Identify the parasite.
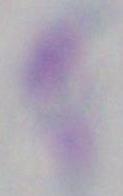
Toxoplasma gondii.

Photomicrograph. 1000x magnification.